Outline each Babesia divergens-infected red blood cell.
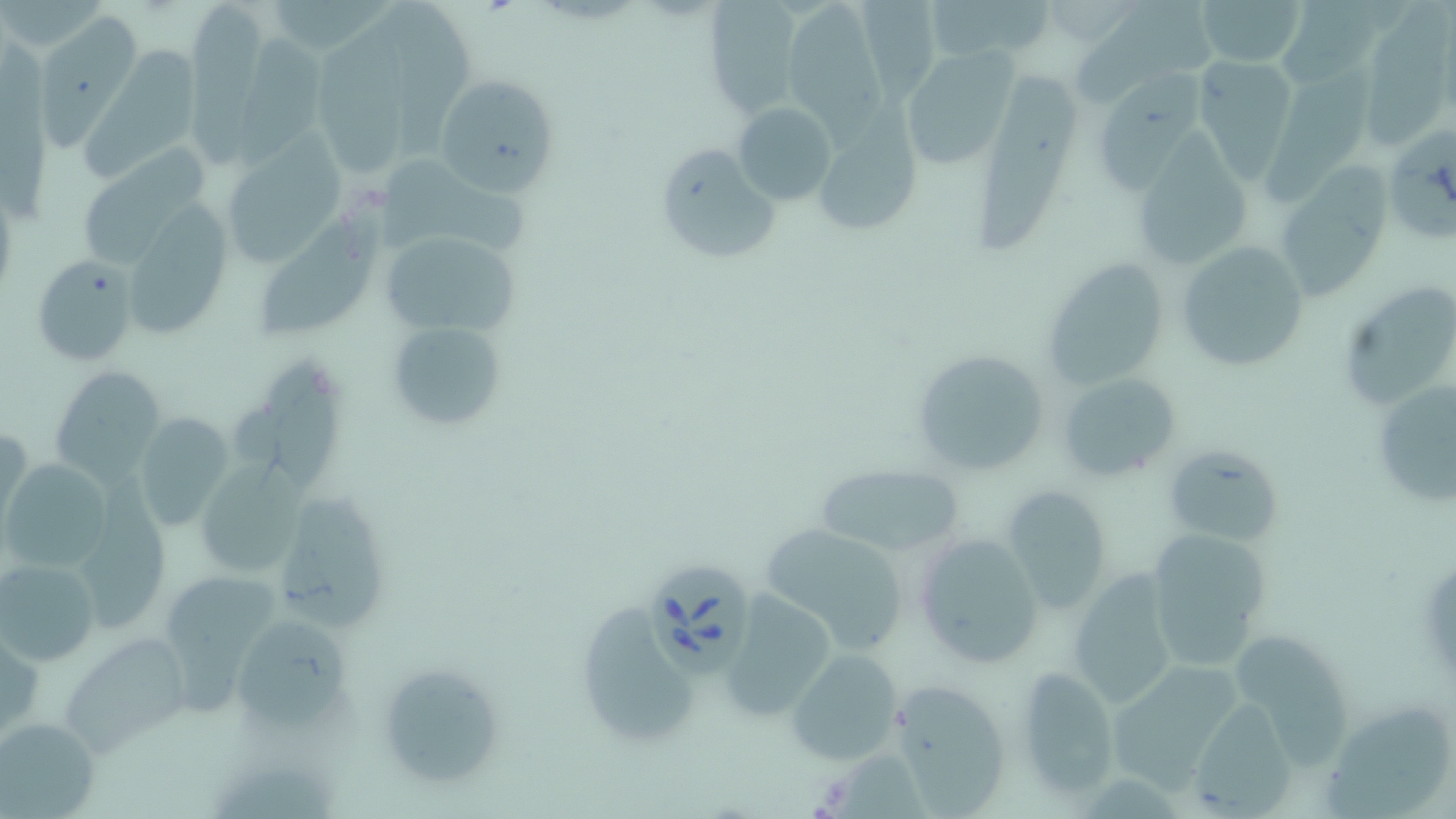

Approximate bounding boxes as (x1,y1)-(x2,y2) corner pairs in pixels.
Babesia divergens-infected red blood cells: (642,556)-(753,681).

Summary:
  - Uninfected red blood cell locations: (183,0)-(272,167), (263,0)-(395,56), (704,0)-(802,116), (922,0)-(1058,64), (1078,0)-(1211,111), (1194,0)-(1307,68), (1281,0)-(1381,83), (783,1)-(895,153), (858,2)-(938,111), (1367,3)-(1442,156), (391,6)-(479,160), (45,17)-(145,151), (315,26)-(416,181), (229,32)-(335,170), (0,38)-(60,228), (74,42)-(201,178), (900,47)-(1021,171), (1192,55)-(1299,183), (1263,65)-(1376,211), (981,67)-(1076,254), (1101,68)-(1194,198), (434,71)-(562,194), (732,102)-(838,208), (809,114)-(920,241), (1389,132)-(1441,248), (218,137)-(344,271), (1128,138)-(1252,275), (654,144)-(776,265), (75,148)-(212,265), (370,154)-(543,260), (1271,161)-(1396,305), (254,200)-(390,338), (133,207)-(236,336), (374,226)-(522,339), (1175,240)-(1311,372), (33,255)-(139,367), (1040,258)-(1174,391), (1342,281)-(1442,413), (386,320)-(508,430), (912,347)-(1051,475), (232,358)-(350,488), (51,366)-(166,483), (1057,372)-(1180,482), (1369,372)-(1456,513), (132,412)-(234,529), (1,423)-(31,528), (1162,442)-(1283,549), (1,459)-(111,571), (192,460)-(307,583), (814,464)-(966,556), (79,475)-(173,634), (1001,484)-(1115,613), (273,488)-(395,629), (760,522)-(913,652), (1146,528)-(1275,667), (912,532)-(1044,668), (1,557)-(100,665), (1064,569)-(1179,708), (162,572)-(284,720), (719,591)-(841,719), (585,603)-(698,743), (235,612)-(354,726), (0,630)-(43,742), (1237,631)-(1353,778), (63,637)-(191,756), (787,650)-(906,766), (372,660)-(508,789), (1104,662)-(1246,790), (1013,665)-(1120,801), (895,678)-(1009,816), (1193,698)-(1296,817), (1324,702)-(1452,817), (0,716)-(101,817)
  - Slide-level diagnosis: Babesia divergens
  - Modality: optical microscopy
  - Image size: 1456×819 pixels
  - Preparation: thin blood smear
  - Stain: May-Grünwald-Giemsa
  - Field of view: single
  - Magnification: 1000x